State which cell type is depicted.
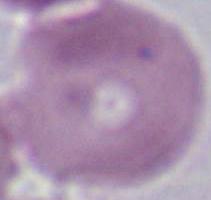

An erythrocyte.

magnification: 1000x
modality: micrograph